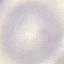
Summary:
  - Malaria status: uninfected
  - Preparation: thin smear
  - Capture: smartphone camera at the microscope eyepiece
  - Image type: automatically extracted cell patch, resized to 64 × 64 pixels
  - Stain: Giemsa